Look for Plasmodium parasites.
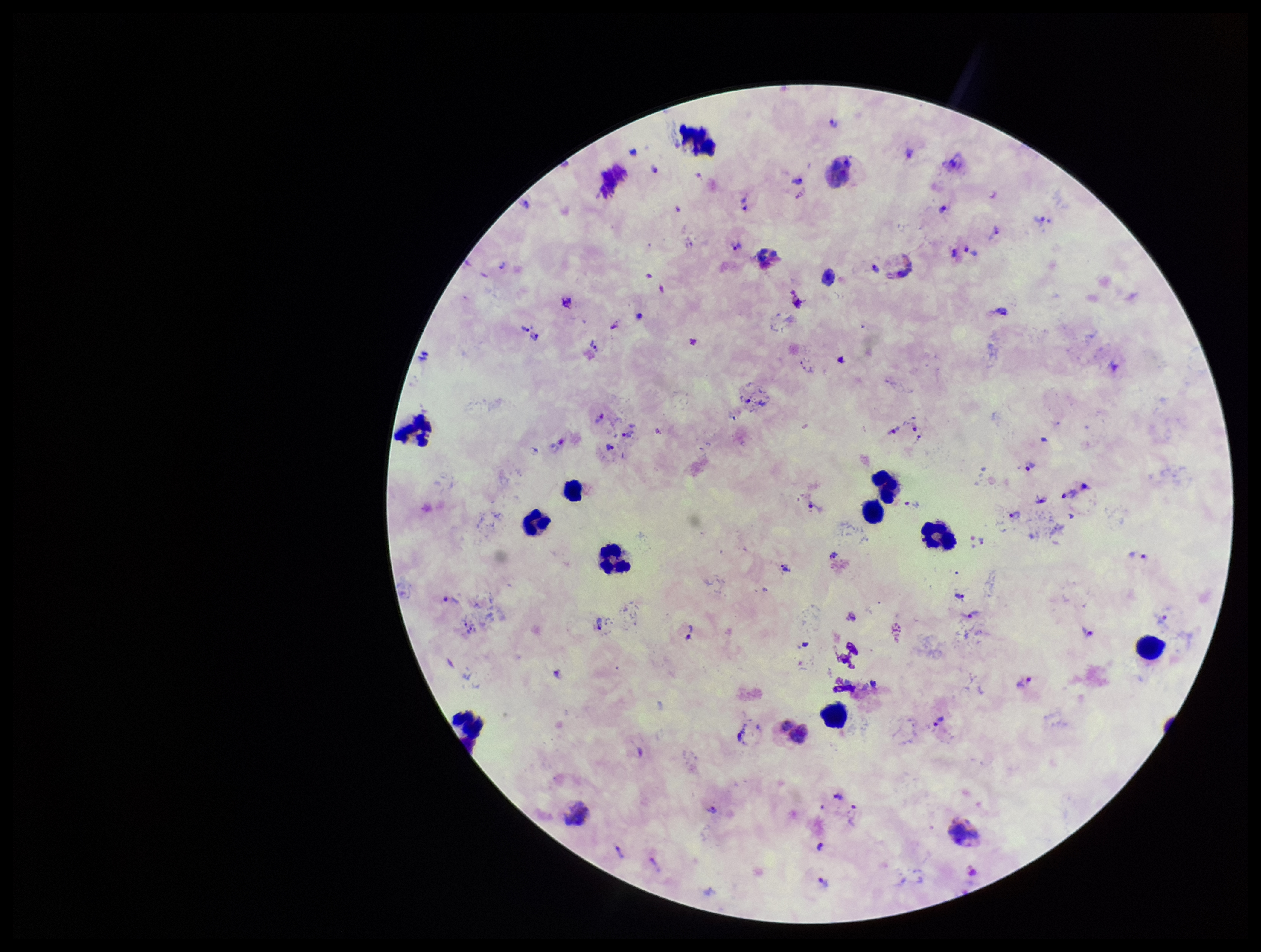
Seen.

parasite count = 44
stain = Giemsa
field of view = single
image size = 1261×952 pixels
leukocyte count = 11
capture = smartphone photograph through the microscope eyepiece
species reported for this patient = Plasmodium vivax
preparation = thick
patient malaria status = positive